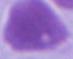
modality: micrograph
magnification: 1000x
identification: erythrocyte